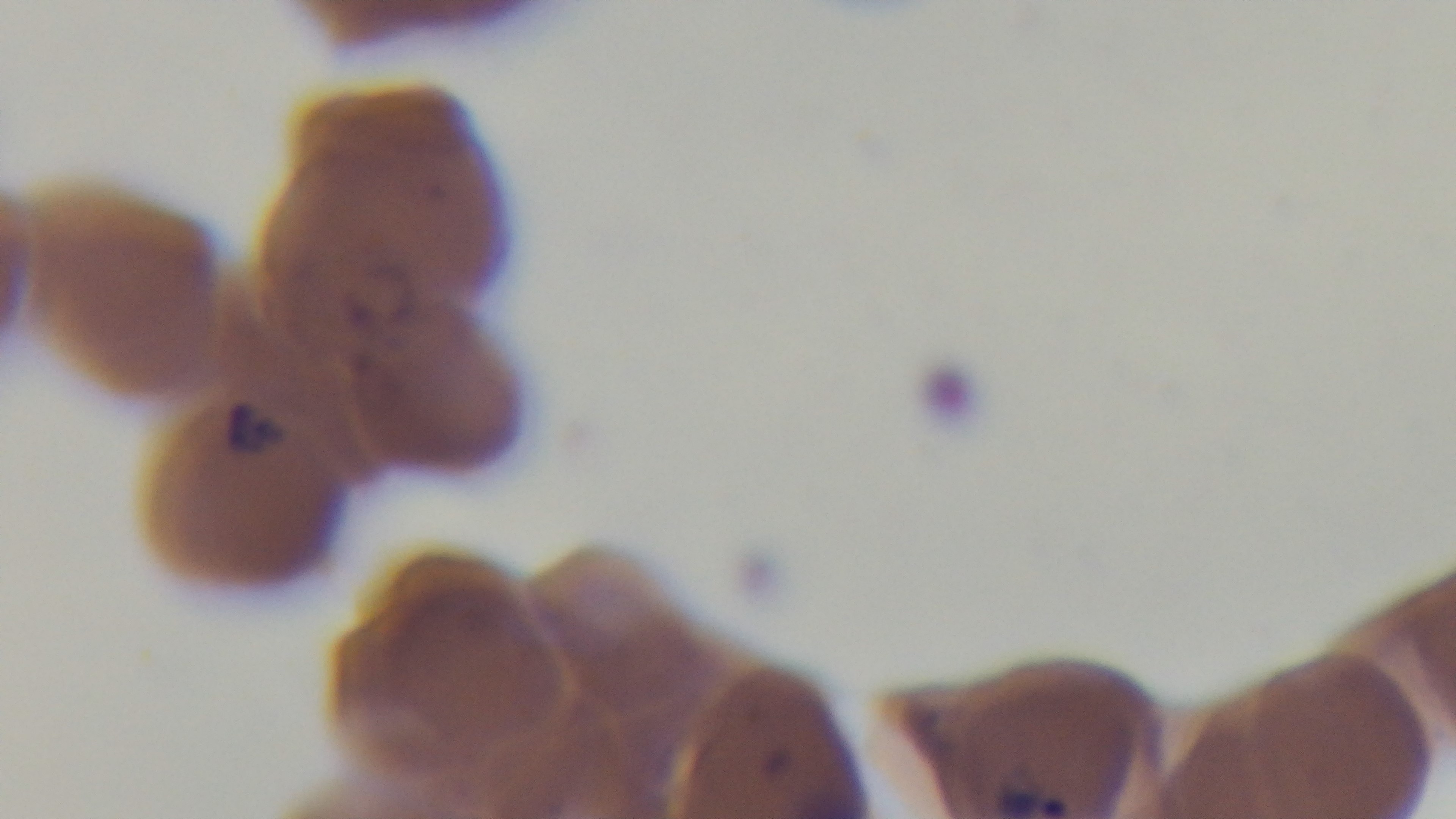

capture: mounted 4K digital camera
field_of_view: one from the slide
objective: 100x oil immersion
malaria_status: infected
stain: Giemsa
modality: light microscopy
preparation: thin blood film